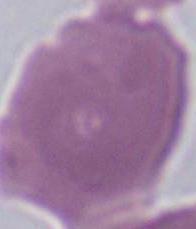 Photomicrograph. 1000x magnification. A red blood cell is seen.